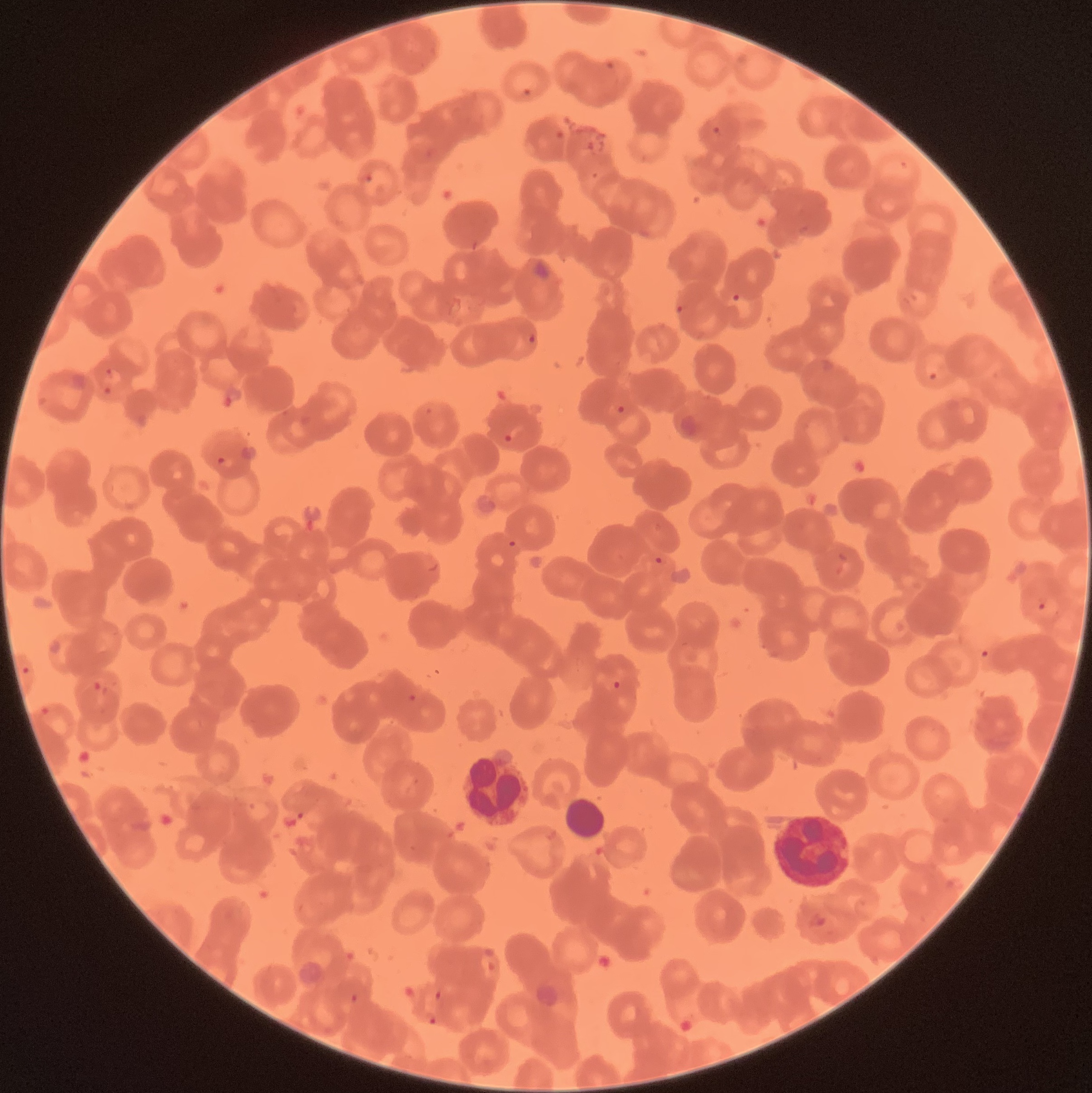

Summary:
  - Coordinate format: approximate bounding boxes as named x1/y1/x2/y2 corners in pixels
  - White blood cell locations: (x1=457, y1=758, x2=533, y2=827), (x1=564, y1=796, x2=607, y2=841), (x1=773, y1=812, x2=855, y2=888)
  - Plasmodium parasite locations: (x1=604, y1=61, x2=617, y2=72), (x1=520, y1=86, x2=536, y2=99), (x1=711, y1=125, x2=723, y2=138), (x1=553, y1=129, x2=564, y2=139), (x1=586, y1=138, x2=607, y2=154), (x1=588, y1=171, x2=602, y2=181), (x1=361, y1=174, x2=375, y2=184), (x1=731, y1=293, x2=742, y2=303), (x1=674, y1=303, x2=687, y2=317), (x1=528, y1=333, x2=536, y2=345), (x1=104, y1=368, x2=114, y2=376), (x1=926, y1=371, x2=938, y2=381), (x1=102, y1=386, x2=112, y2=396), (x1=615, y1=404, x2=627, y2=415), (x1=503, y1=433, x2=514, y2=444), (x1=216, y1=456, x2=235, y2=470), (x1=507, y1=539, x2=517, y2=549), (x1=654, y1=556, x2=664, y2=566), (x1=1036, y1=595, x2=1049, y2=611), (x1=977, y1=648, x2=992, y2=661), (x1=20, y1=665, x2=31, y2=676), (x1=612, y1=679, x2=622, y2=690), (x1=91, y1=680, x2=104, y2=693), (x1=408, y1=693, x2=416, y2=702), (x1=39, y1=706, x2=55, y2=716), (x1=806, y1=912, x2=828, y2=931), (x1=434, y1=989, x2=443, y2=1001), (x1=349, y1=991, x2=360, y2=1002), (x1=428, y1=1016, x2=438, y2=1026)
  - Image size: 1092×1093 pixels
  - Modality: light microscopy
  - Preparation: thin blood film
  - Red blood cell morphology: rouleaux formation